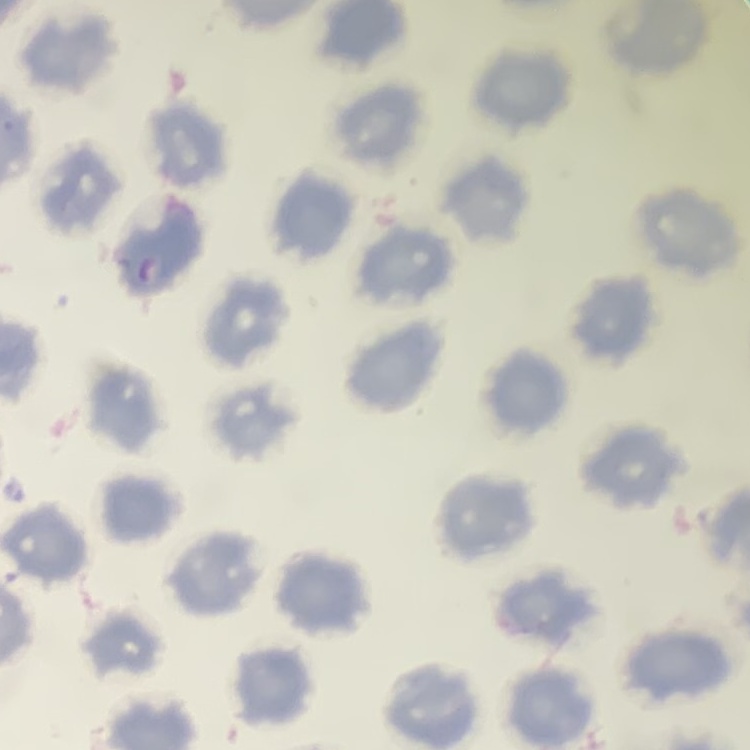

{
  "erythrocyte_morphology": "no rouleaux formation",
  "preparation": "thin blood film",
  "image_type": "one tile cut from a larger photomicrograph",
  "stain": "Field's or Giemsa"
}